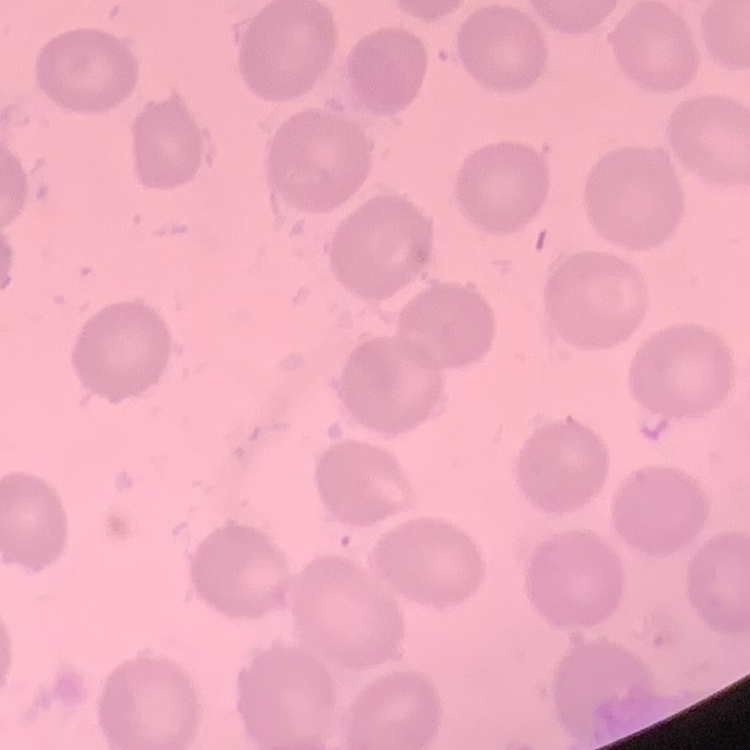
Summary:
  - Erythrocyte morphology: no rouleaux formation
  - Image type: one tile cut from a larger photomicrograph
  - Preparation: thin blood film
  - Stain: Field's or Giemsa